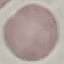

Summary:
  - Result: negative for malaria parasites
  - Capture: smartphone camera at the microscope eyepiece
  - Stain: Giemsa
  - Image type: automatically extracted cell patch, resized to 64 × 64 pixels
  - Preparation: thin blood film